Give the extent of all uninfected red blood cells.
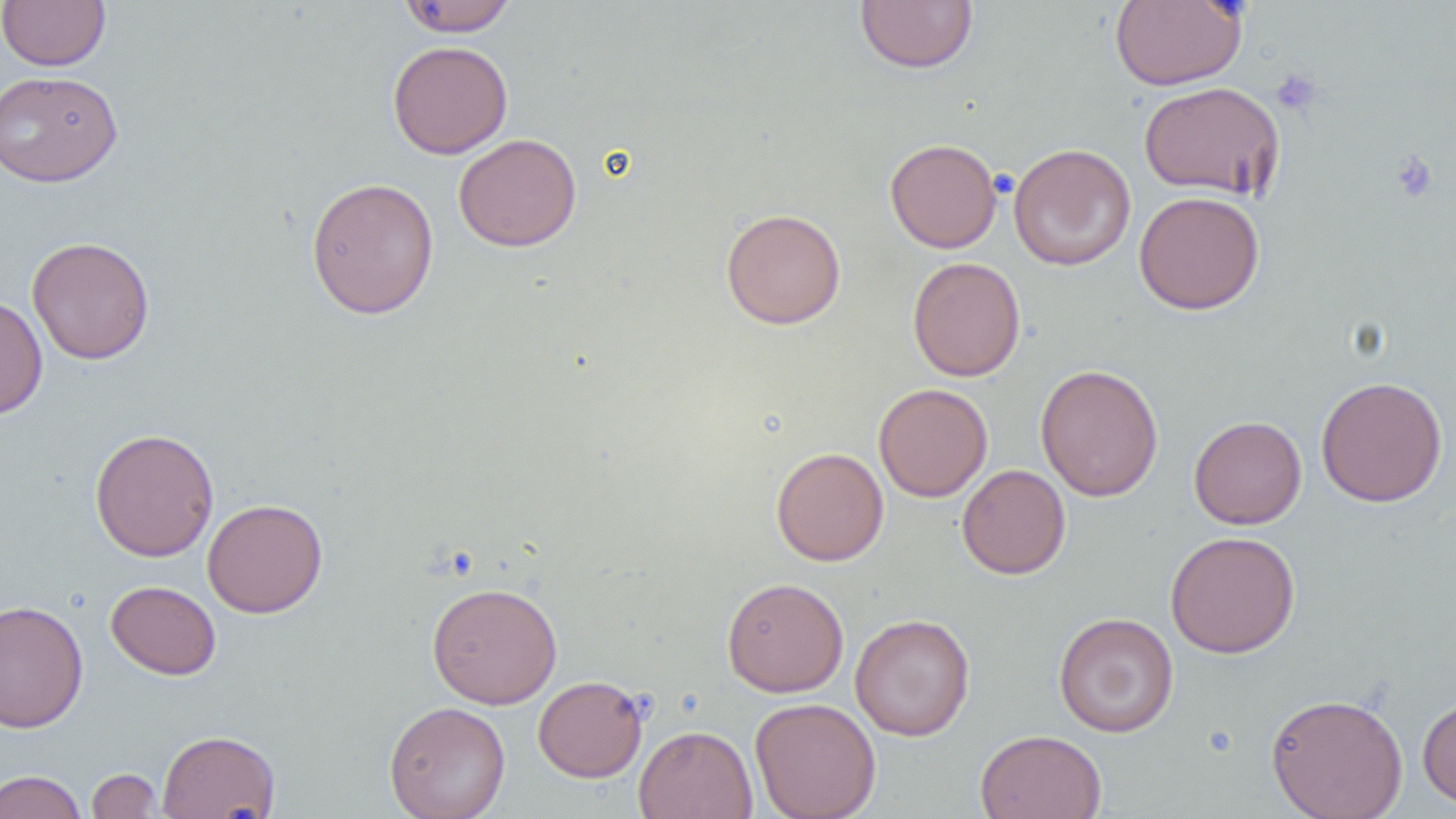

Approximate bounding boxes as (x1, y1, x2, y2) in pixels.
Uninfected red blood cells: (0, 0, 111, 71), (397, 0, 519, 37), (854, 0, 979, 74), (1110, 0, 1247, 90), (387, 40, 513, 159), (0, 69, 123, 187), (1139, 81, 1285, 201), (453, 133, 582, 251), (885, 138, 1001, 253), (1008, 143, 1136, 271), (306, 176, 439, 320), (1134, 190, 1265, 315), (720, 207, 846, 329), (26, 235, 155, 366), (907, 256, 1026, 381), (0, 294, 48, 419), (1035, 363, 1164, 502), (1316, 376, 1448, 507), (873, 383, 992, 502), (1189, 415, 1307, 530), (89, 427, 219, 562), (771, 447, 889, 566), (957, 464, 1071, 579), (202, 498, 328, 618), (1165, 531, 1301, 658), (722, 577, 849, 697), (106, 580, 221, 680), (427, 580, 563, 709), (0, 599, 89, 734), (1053, 611, 1179, 737), (850, 613, 975, 741), (533, 675, 648, 782), (1266, 692, 1408, 818), (1417, 696, 1456, 810), (750, 697, 881, 819), (384, 700, 511, 819), (634, 725, 758, 819), (157, 729, 281, 818), (975, 729, 1107, 819), (86, 768, 162, 818), (0, 770, 87, 819).

Platelet locations: (1270, 68, 1323, 116), (1389, 150, 1439, 203), (990, 168, 1018, 199). Slide-level diagnosis: negative for blood parasites. Light microscopy. Thin blood film. 1000x magnification. Image is 1456×819 pixels. Single field of view.